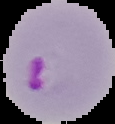
Malaria status: parasitized. Segmented cell region on a black background. Image is 115×124 pixels. From a thin blood smear.